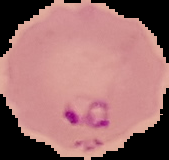

Result: Plasmodium parasites identified. From a thin blood film. Segmented cell region on a black background. Image is 169×160 pixels.